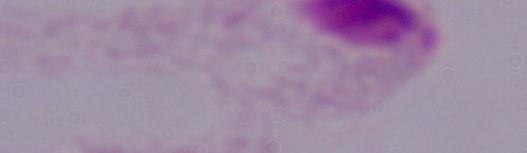

Summary:
  - Modality: photomicrograph
  - Identification: trichomonad
  - Magnification: 1000x